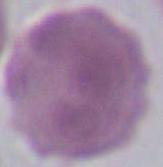

magnification = 1000x
identification = red blood cell
modality = photomicrograph